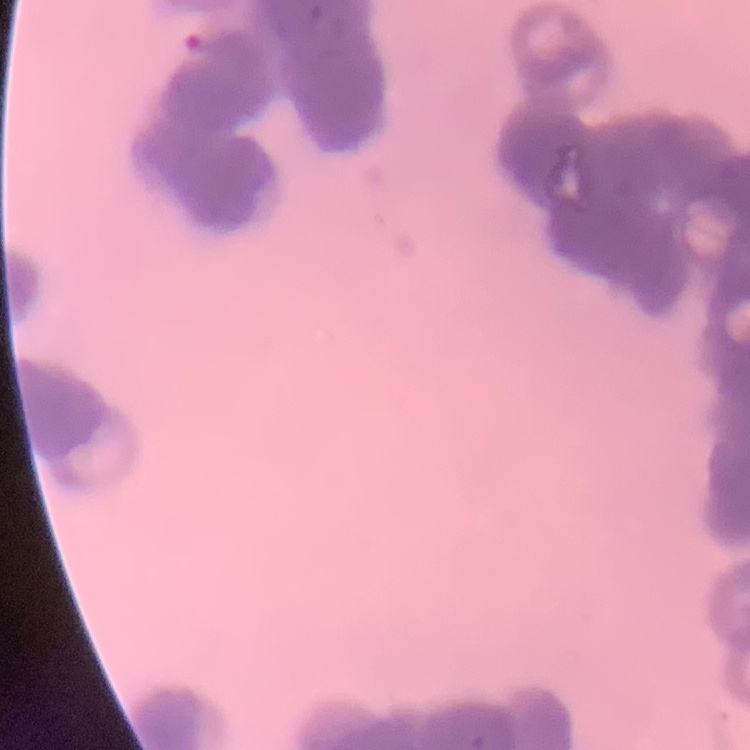
The red blood cells exhibit rouleaux formation. One tile cut from a larger photomicrograph. Field's or Giemsa stain. Thin peripheral smear.